Locate and identify every blood parasite.
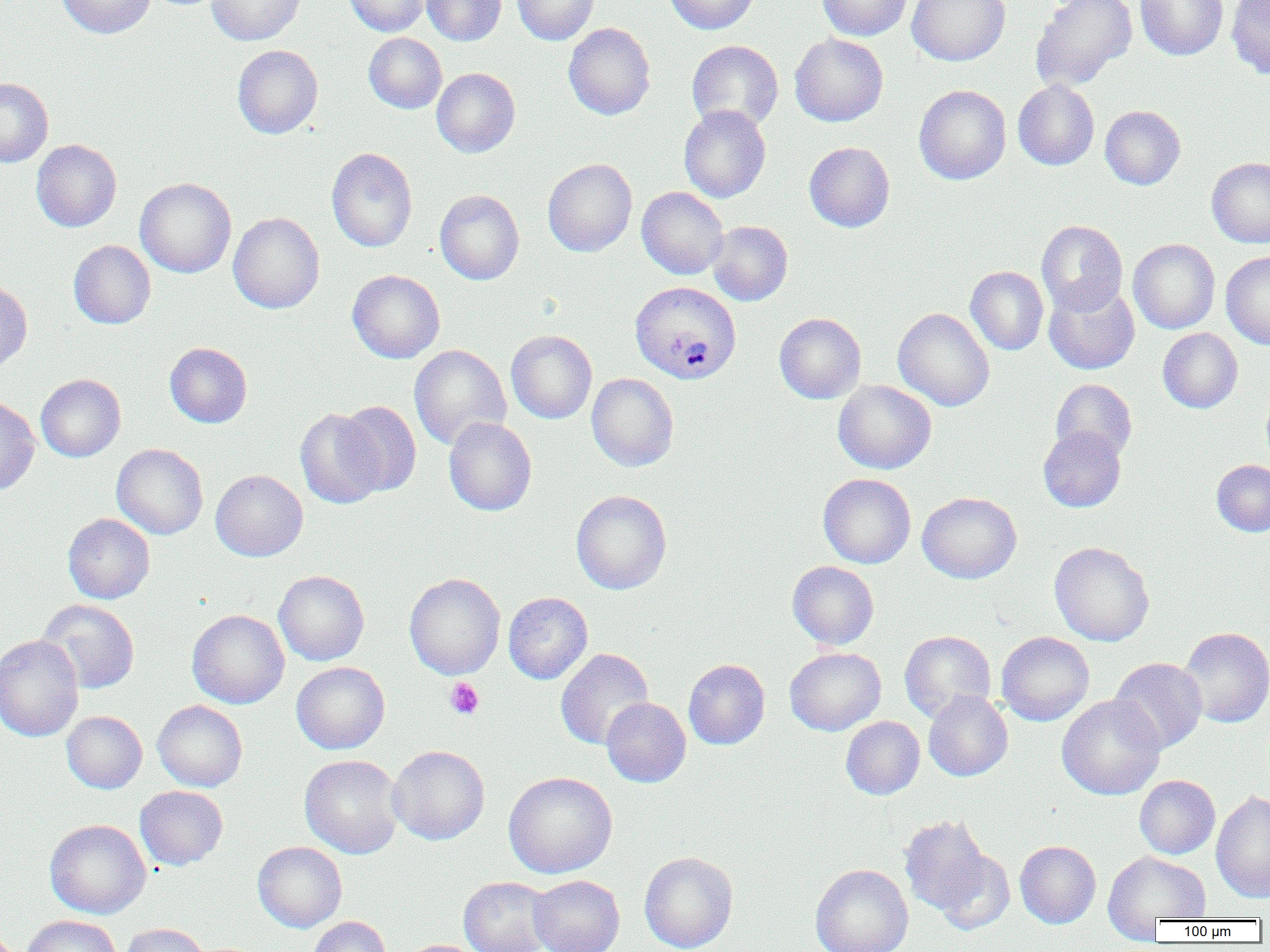
Approximate bounding boxes as (x1,y1)-(x2,y2) corner pairs in pixels.
Plasmodium vivax-infected red blood cells: (630,281)-(741,384).
No Plasmodium falciparum, Plasmodium ovale, Plasmodium malariae, Babesia divergens, or Trypanosoma brucei observed.

slide_level_diagnosis: Plasmodium vivax
preparation: thin blood smear
platelet_locations: 'approximate bounding boxes as (x1,y1)-(x2,y2) corner pairs in pixels: (445,678)-(484,719)'
image_size: 1270×952 pixels
field_of_view: single
modality: light microscopy
uninfected_red_blood_cell_locations: 'approximate bounding boxes as (x1,y1)-(x2,y2) corner pairs in pixels: (57,0)-(155,38), (207,0)-(305,45), (344,0)-(430,36), (422,0)-(506,46), (512,0)-(600,45), (664,0)-(760,34), (817,0)-(914,41), (907,0)-(1010,66), (1030,0)-(1137,92), (1135,0)-(1228,61), (1226,0)-(1270,80), (563,22)-(655,120), (363,33)-(447,113), (790,33)-(888,126), (686,40)-(784,132), (232,45)-(323,138), (432,67)-(520,157), (0,77)-(53,167), (1013,80)-(1099,170), (914,84)-(1011,185), (679,105)-(771,203), (1100,105)-(1185,190), (31,139)-(121,232), (804,142)-(895,232), (326,147)-(418,252), (1206,157)-(1270,247), (542,158)-(637,256), (135,178)-(236,278), (637,187)-(728,279), (435,190)-(524,285), (228,212)-(325,313), (1036,220)-(1127,314), (708,221)-(793,306), (1128,239)-(1220,333), (68,240)-(156,329), (1221,251)-(1270,349), (965,266)-(1049,355), (347,269)-(445,363), (0,279)-(32,373), (1043,280)-(1140,375), (893,307)-(994,411), (774,313)-(866,404), (1158,328)-(1243,413), (506,330)-(597,423), (164,342)-(252,428), (409,344)-(511,450), (586,373)-(679,471), (35,374)-(126,462), (833,379)-(936,474), (1050,379)-(1137,462), (1262,386)-(1270,469), (0,395)-(40,495), (335,400)-(422,498), (295,407)-(387,509), (444,417)-(537,516), (1038,427)-(1126,512), (111,443)-(208,539), (1211,459)-(1270,536), (211,470)-(308,561), (818,473)-(916,568), (571,489)-(672,594), (917,492)-(1021,584), (62,513)-(154,604), (1050,542)-(1154,646), (787,561)-(879,650), (274,570)-(369,665), (404,573)-(505,679), (503,592)-(593,684), (37,599)-(140,694), (187,609)-(289,709), (1178,627)-(1270,728), (899,630)-(996,721), (997,631)-(1094,725), (0,635)-(84,742), (785,647)-(886,735), (555,648)-(654,751), (1110,657)-(1207,754), (683,659)-(770,750), (291,661)-(390,753), (923,690)-(1013,781), (1057,694)-(1166,800), (601,697)-(691,787), (152,700)-(248,792), (62,711)-(147,793), (841,716)-(925,800), (387,745)-(489,844), (300,754)-(404,858), (503,771)-(617,878), (1134,775)-(1220,859), (135,786)-(228,870), (1211,788)-(1270,904), (899,815)-(991,916), (44,819)-(151,919), (1015,840)-(1101,928), (252,842)-(347,932), (933,848)-(1015,934), (1103,850)-(1211,933), (639,851)-(738,952), (810,863)-(914,952), (529,874)-(625,952), (459,876)-(553,952), (22,915)-(122,952), (306,916)-(392,952), (119,923)-(212,952), (399,939)-(484,952)'
magnification: 1000x